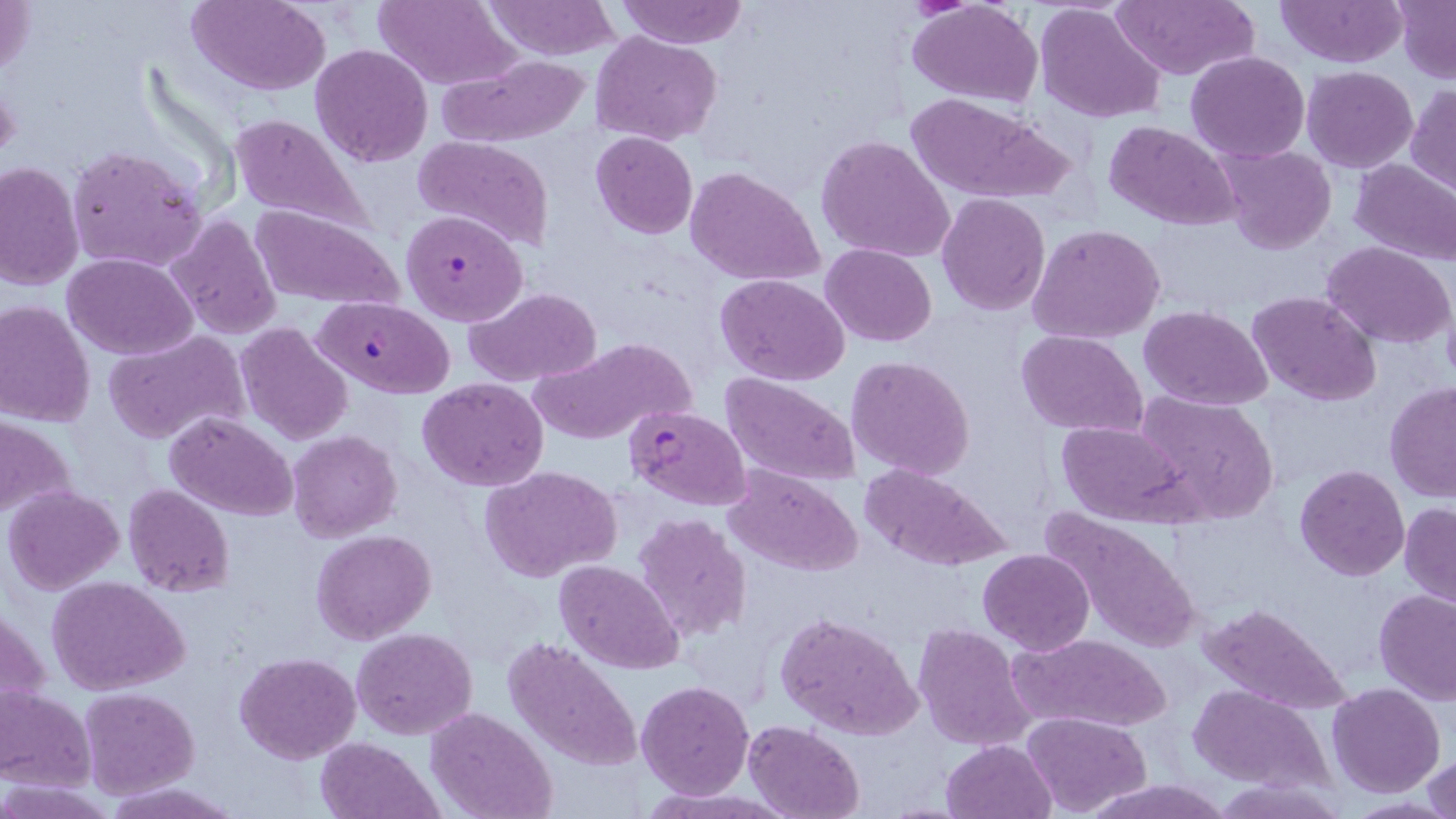
slide-level diagnosis = Plasmodium falciparum
field of view = single
modality = light microscopy
preparation = thin blood smear
magnification = 1000x
image size = 1456×819 pixels
stain = May-Grünwald-Giemsa
uninfected red blood cell locations = approximate bounding boxes as (x1, y1, x2, y2) in pixels: (1, 0, 37, 83), (187, 0, 331, 94), (484, 0, 621, 61), (617, 0, 747, 47), (907, 0, 1044, 108), (1276, 0, 1406, 67), (373, 1, 521, 89), (1035, 2, 1166, 122), (1111, 2, 1258, 80), (1395, 2, 1455, 81), (592, 31, 721, 145), (309, 44, 433, 167), (436, 50, 592, 147), (1185, 50, 1310, 163), (1301, 66, 1418, 172), (1406, 84, 1456, 199), (906, 94, 1074, 204), (229, 113, 380, 241), (1104, 121, 1240, 230), (591, 131, 698, 239), (815, 134, 955, 264), (412, 136, 554, 253), (1214, 143, 1337, 256), (64, 146, 207, 274), (1349, 158, 1456, 266), (0, 160, 84, 290), (684, 166, 826, 288), (937, 194, 1050, 316), (249, 204, 402, 311), (167, 214, 284, 339), (1028, 224, 1167, 347), (1324, 242, 1456, 348), (819, 244, 938, 347), (64, 252, 198, 359), (717, 274, 850, 386), (465, 287, 605, 386), (1248, 290, 1383, 407), (0, 300, 97, 427), (1140, 305, 1274, 412), (235, 322, 354, 446), (103, 330, 250, 445), (1016, 330, 1148, 438), (529, 336, 695, 446), (846, 354, 977, 480), (721, 374, 860, 487), (418, 378, 548, 491), (1384, 382, 1456, 503), (1134, 390, 1282, 523), (165, 411, 296, 520), (0, 413, 78, 523), (1056, 419, 1192, 525), (287, 430, 401, 541), (857, 462, 1012, 571), (481, 464, 625, 582), (722, 464, 864, 579), (1295, 465, 1409, 581), (652, 481, 845, 604), (122, 484, 236, 598), (4, 485, 125, 595), (1399, 502, 1456, 610), (1037, 506, 1203, 656), (633, 513, 753, 644), (311, 529, 436, 644), (978, 549, 1095, 655), (557, 560, 682, 675), (47, 576, 190, 695), (1374, 590, 1456, 705), (2, 600, 46, 727), (1199, 601, 1350, 714), (774, 608, 922, 740), (912, 624, 1036, 750), (351, 627, 478, 739), (1010, 631, 1174, 733), (503, 637, 643, 772), (235, 651, 361, 763), (637, 681, 754, 799), (1327, 684, 1446, 797), (1188, 686, 1329, 789), (0, 687, 97, 788), (78, 688, 200, 798), (428, 708, 556, 819), (1019, 712, 1152, 815), (743, 719, 866, 819), (316, 736, 441, 819), (941, 738, 1056, 819), (1424, 755, 1455, 819), (1219, 777, 1346, 817), (0, 778, 115, 817), (1085, 778, 1227, 817), (105, 781, 239, 817)
Plasmodium falciparum-infected red blood cell locations = approximate bounding boxes as (x1, y1, x2, y2) in pixels: (400, 209, 526, 326), (311, 297, 455, 398), (623, 404, 752, 510)